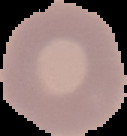

Summary:
  - Preparation: thin blood film
  - Image type: segmented cell region with the area outside set to black
  - Result: negative for Plasmodium parasites
  - Image size: 127×136 pixels